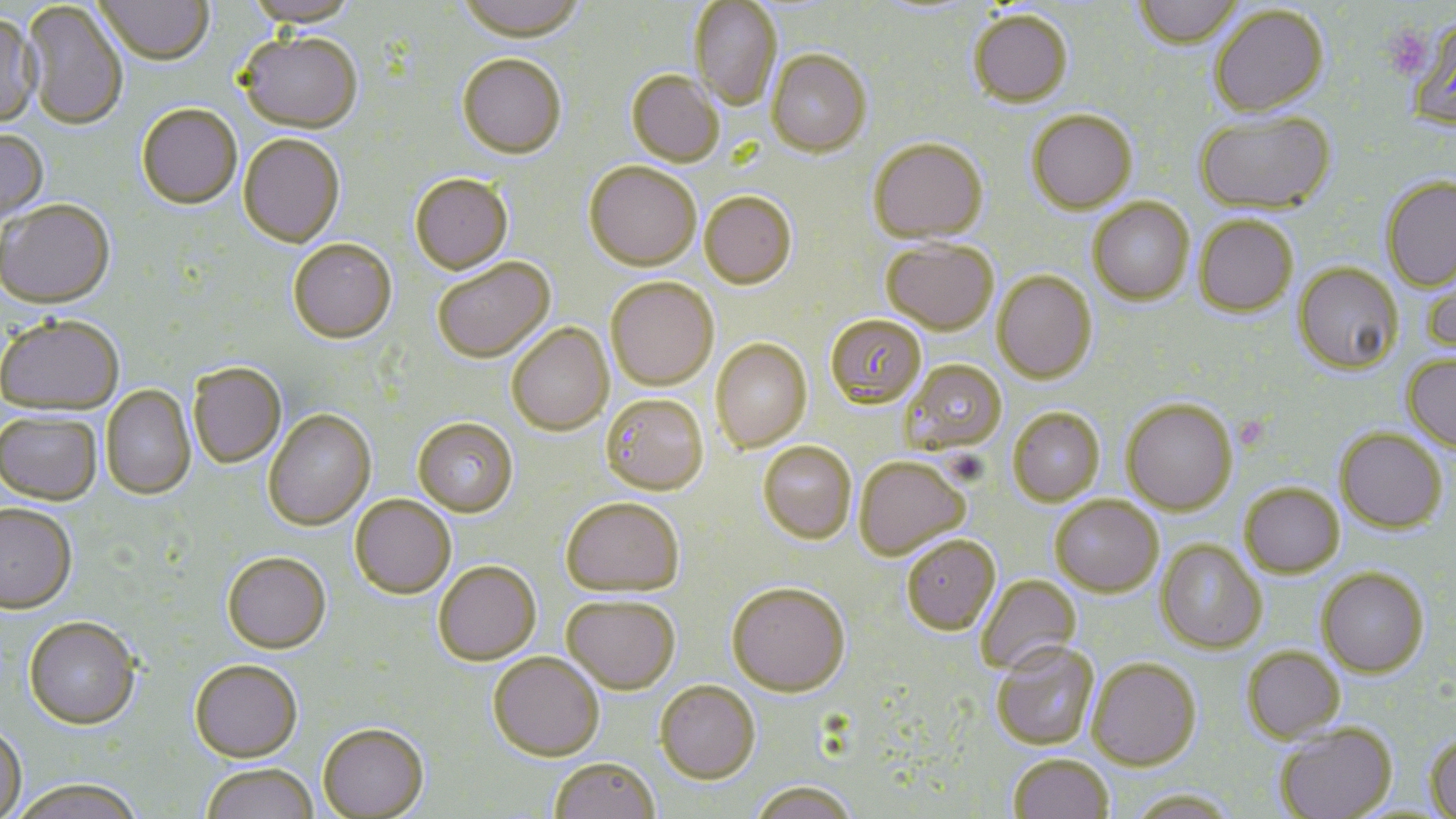

Summary:
  - Coordinate format: approximate bounding boxes as (x1,y1)-(x2,y2) corner pairs in pixels
  - Uninfected red blood cell locations: (93,0)-(213,68), (244,0)-(359,29), (455,0)-(586,46), (1133,0)-(1244,51), (688,1)-(782,110), (21,2)-(128,133), (1210,6)-(1329,119), (968,12)-(1073,110), (0,15)-(43,130), (1408,17)-(1456,133), (236,34)-(362,136), (766,51)-(871,158), (457,56)-(567,160), (626,71)-(725,167), (137,106)-(242,211), (1027,111)-(1138,215), (1195,111)-(1336,216), (0,129)-(48,226), (238,135)-(346,250), (869,140)-(988,245), (585,161)-(702,272), (410,174)-(513,276), (1381,176)-(1456,293), (700,191)-(797,289), (1088,199)-(1194,306), (0,201)-(116,310), (1194,215)-(1298,317), (882,239)-(999,335), (288,240)-(397,345), (432,257)-(555,363), (1422,257)-(1456,358), (1294,263)-(1402,375), (992,272)-(1097,384), (606,277)-(719,390), (824,314)-(927,410), (0,317)-(124,417), (507,323)-(614,436), (712,339)-(812,452), (1403,355)-(1456,452), (902,359)-(1008,453), (188,364)-(287,469), (101,386)-(196,501), (601,393)-(708,495), (1121,399)-(1237,515), (1008,408)-(1104,506), (264,410)-(376,531), (0,411)-(102,506), (413,417)-(519,517), (1335,428)-(1447,533), (758,441)-(857,544), (854,456)-(970,560), (1240,483)-(1344,578), (1050,495)-(1163,597), (350,496)-(456,599), (561,497)-(684,597), (0,504)-(78,615), (901,535)-(1001,635), (1156,539)-(1266,653), (222,552)-(331,654), (433,561)-(542,666), (1316,567)-(1429,677), (976,574)-(1082,675), (727,581)-(851,696), (561,595)-(680,694), (23,617)-(141,729), (991,641)-(1099,750), (1241,646)-(1345,742), (488,652)-(605,760), (1087,658)-(1201,770), (190,659)-(302,762), (655,680)-(760,783), (317,723)-(430,818), (0,724)-(27,819), (1275,724)-(1396,819), (1425,732)-(1456,817), (1009,753)-(1113,819), (549,757)-(660,819), (200,763)-(318,819), (10,779)-(145,819), (750,780)-(859,819), (1128,790)-(1238,819)
  - Slide-level diagnosis: Plasmodium falciparum
  - Magnification: 1000x
  - Preparation: thin blood smear
  - Modality: light microscopy
  - Field of view: one of a larger specimen
  - Stain: May-Grünwald-Giemsa
  - Image size: 1456×819 pixels